Classify this cell by malaria status.
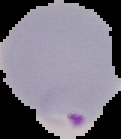

Parasitized.

From a thin blood smear. Image is 121×139 pixels. Cell region segmented out of the field of view; the surrounding area is masked to black.